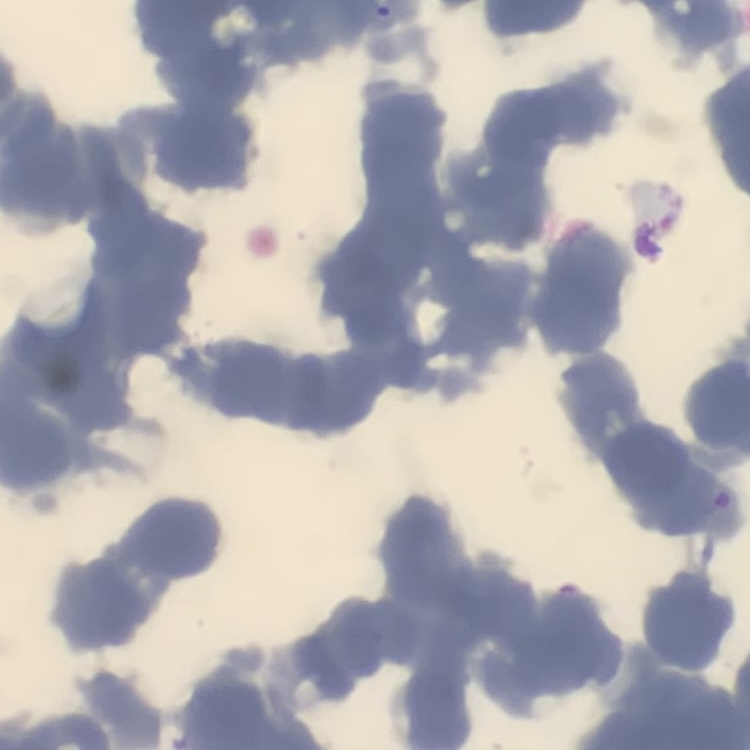

The erythrocytes exhibit rouleaux formation. Thin blood film. Square crop of a larger photomicrograph. Field's or Giemsa stain.